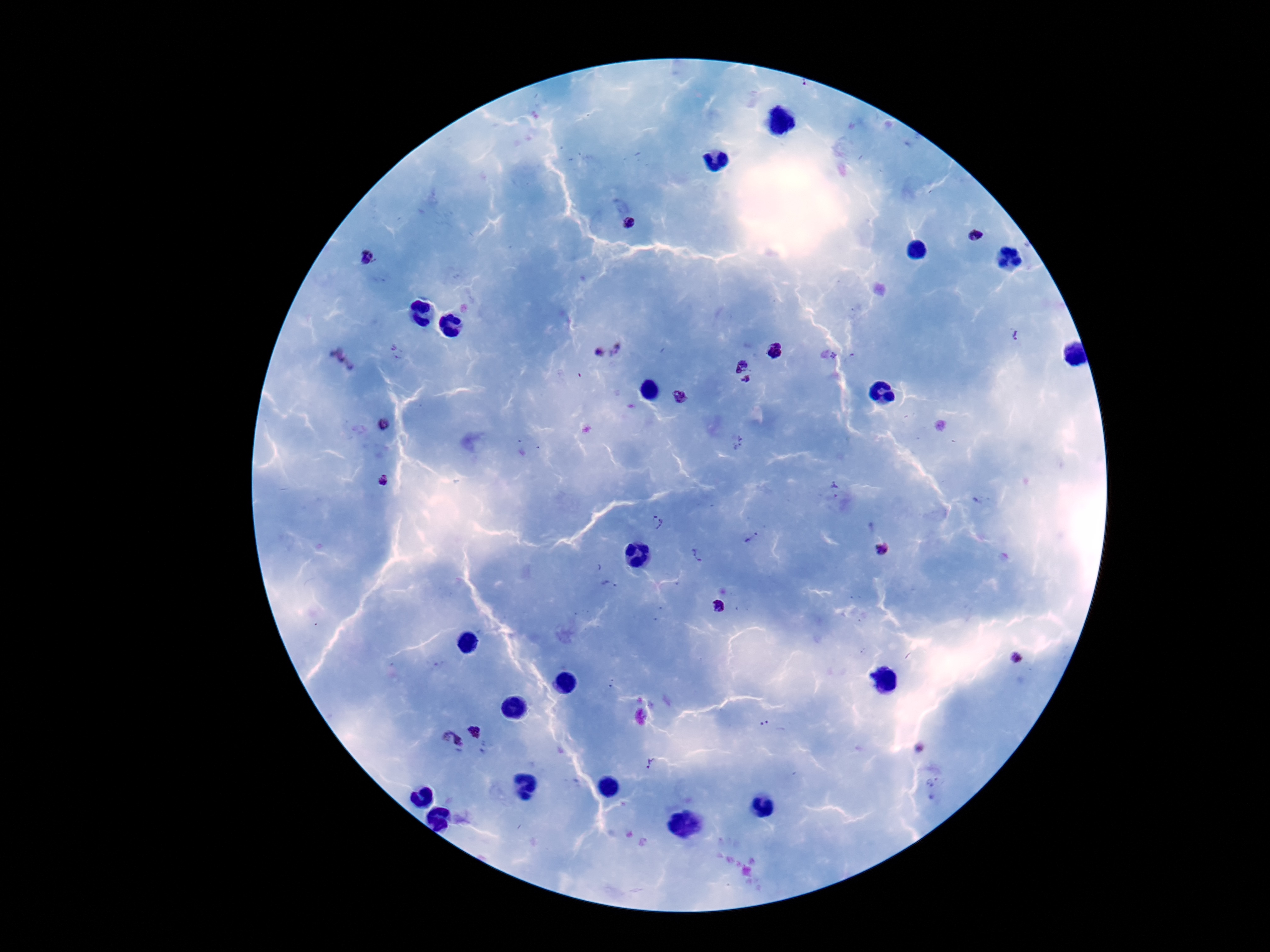

stain = Giemsa
patient malaria status = infected
capture = smartphone camera through the microscope eyepiece
field of view = single
image size = 1270×952 pixels
magnification = 100x
preparation = thick blood film
Plasmodium parasite locations = approximate centers as (x, y) in pixels: (629, 223), (980, 237), (366, 257), (1016, 336), (620, 348), (598, 352), (776, 352), (834, 356), (342, 362), (741, 364), (747, 381), (680, 396), (384, 426), (382, 480), (836, 490), (658, 523), (751, 538), (883, 549), (698, 557), (719, 606), (1014, 659), (764, 724), (476, 730), (450, 742), (650, 764), (934, 780)